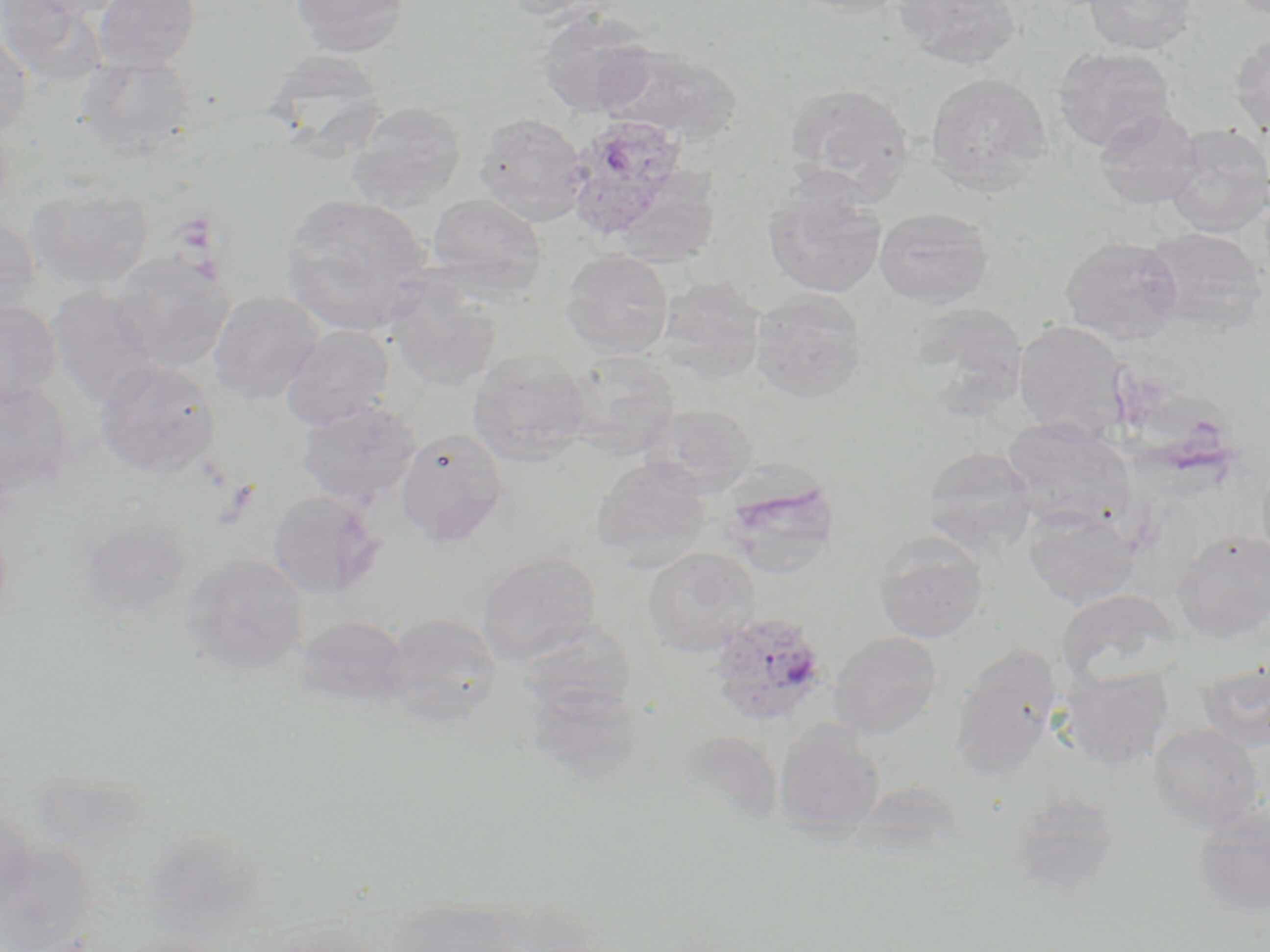

{
  "slide_level_diagnosis": "Plasmodium ovale",
  "modality": "optical microscopy",
  "field_of_view": "single",
  "platelet_locations": "approximate bounding boxes as named x1/y1/x2/y2 corners in pixels: (x1=217, y1=478, x2=259, y2=525)",
  "magnification": "1000x",
  "plasmodium_ovale_infected_red_blood_cell_locations": "approximate bounding boxes as named x1/y1/x2/y2 corners in pixels: (x1=564, y1=114, x2=690, y2=239), (x1=707, y1=612, x2=830, y2=727)",
  "uninfected_red_blood_cell_locations": "approximate bounding boxes as named x1/y1/x2/y2 corners in pixels: (x1=0, y1=0, x2=102, y2=84), (x1=17, y1=0, x2=132, y2=19), (x1=94, y1=0, x2=200, y2=72), (x1=289, y1=0, x2=413, y2=56), (x1=499, y1=0, x2=615, y2=20), (x1=788, y1=0, x2=914, y2=18), (x1=893, y1=0, x2=1022, y2=69), (x1=1084, y1=0, x2=1197, y2=55), (x1=537, y1=9, x2=657, y2=118), (x1=0, y1=30, x2=33, y2=140), (x1=1230, y1=33, x2=1270, y2=136), (x1=598, y1=43, x2=741, y2=146), (x1=1052, y1=46, x2=1176, y2=152), (x1=262, y1=48, x2=389, y2=153), (x1=79, y1=53, x2=197, y2=158), (x1=925, y1=72, x2=1051, y2=193), (x1=784, y1=82, x2=914, y2=198), (x1=348, y1=101, x2=467, y2=211), (x1=1094, y1=108, x2=1203, y2=210), (x1=474, y1=112, x2=587, y2=226), (x1=1165, y1=125, x2=1270, y2=236), (x1=762, y1=178, x2=887, y2=299), (x1=25, y1=187, x2=154, y2=292), (x1=427, y1=192, x2=547, y2=295), (x1=279, y1=194, x2=432, y2=335), (x1=874, y1=206, x2=993, y2=308), (x1=0, y1=212, x2=40, y2=321), (x1=1141, y1=227, x2=1268, y2=336), (x1=1060, y1=235, x2=1184, y2=343), (x1=561, y1=248, x2=675, y2=360), (x1=110, y1=250, x2=235, y2=372), (x1=385, y1=276, x2=502, y2=393), (x1=655, y1=276, x2=767, y2=385), (x1=47, y1=288, x2=160, y2=408), (x1=750, y1=288, x2=869, y2=403), (x1=208, y1=291, x2=323, y2=406), (x1=0, y1=300, x2=61, y2=404), (x1=1013, y1=319, x2=1133, y2=441), (x1=282, y1=324, x2=394, y2=430), (x1=467, y1=350, x2=591, y2=467), (x1=562, y1=350, x2=681, y2=460), (x1=94, y1=359, x2=221, y2=478), (x1=0, y1=380, x2=75, y2=494), (x1=297, y1=398, x2=421, y2=506), (x1=639, y1=404, x2=759, y2=496), (x1=1002, y1=417, x2=1137, y2=530), (x1=396, y1=427, x2=510, y2=548), (x1=923, y1=446, x2=1037, y2=552), (x1=590, y1=455, x2=711, y2=567), (x1=720, y1=474, x2=841, y2=580), (x1=267, y1=490, x2=382, y2=600), (x1=1023, y1=504, x2=1142, y2=610), (x1=78, y1=514, x2=193, y2=620), (x1=1173, y1=529, x2=1270, y2=641), (x1=873, y1=531, x2=988, y2=643), (x1=641, y1=547, x2=760, y2=656), (x1=477, y1=551, x2=601, y2=665), (x1=181, y1=553, x2=309, y2=676), (x1=1054, y1=588, x2=1185, y2=687), (x1=382, y1=612, x2=502, y2=726), (x1=296, y1=615, x2=411, y2=710), (x1=518, y1=621, x2=638, y2=718), (x1=828, y1=631, x2=944, y2=738), (x1=949, y1=645, x2=1063, y2=779), (x1=1197, y1=661, x2=1270, y2=752), (x1=1058, y1=668, x2=1173, y2=770), (x1=518, y1=679, x2=643, y2=784), (x1=774, y1=721, x2=886, y2=837), (x1=1147, y1=723, x2=1265, y2=832), (x1=680, y1=730, x2=783, y2=831), (x1=1009, y1=792, x2=1123, y2=902), (x1=1191, y1=804, x2=1270, y2=919), (x1=0, y1=807, x2=36, y2=911), (x1=143, y1=829, x2=264, y2=937), (x1=0, y1=842, x2=97, y2=952), (x1=385, y1=902, x2=524, y2=952), (x1=258, y1=919, x2=382, y2=952), (x1=112, y1=935, x2=230, y2=952)",
  "preparation": "thin blood smear",
  "image_size": "1270×952 pixels",
  "stain": "May-Grünwald-Giemsa"
}